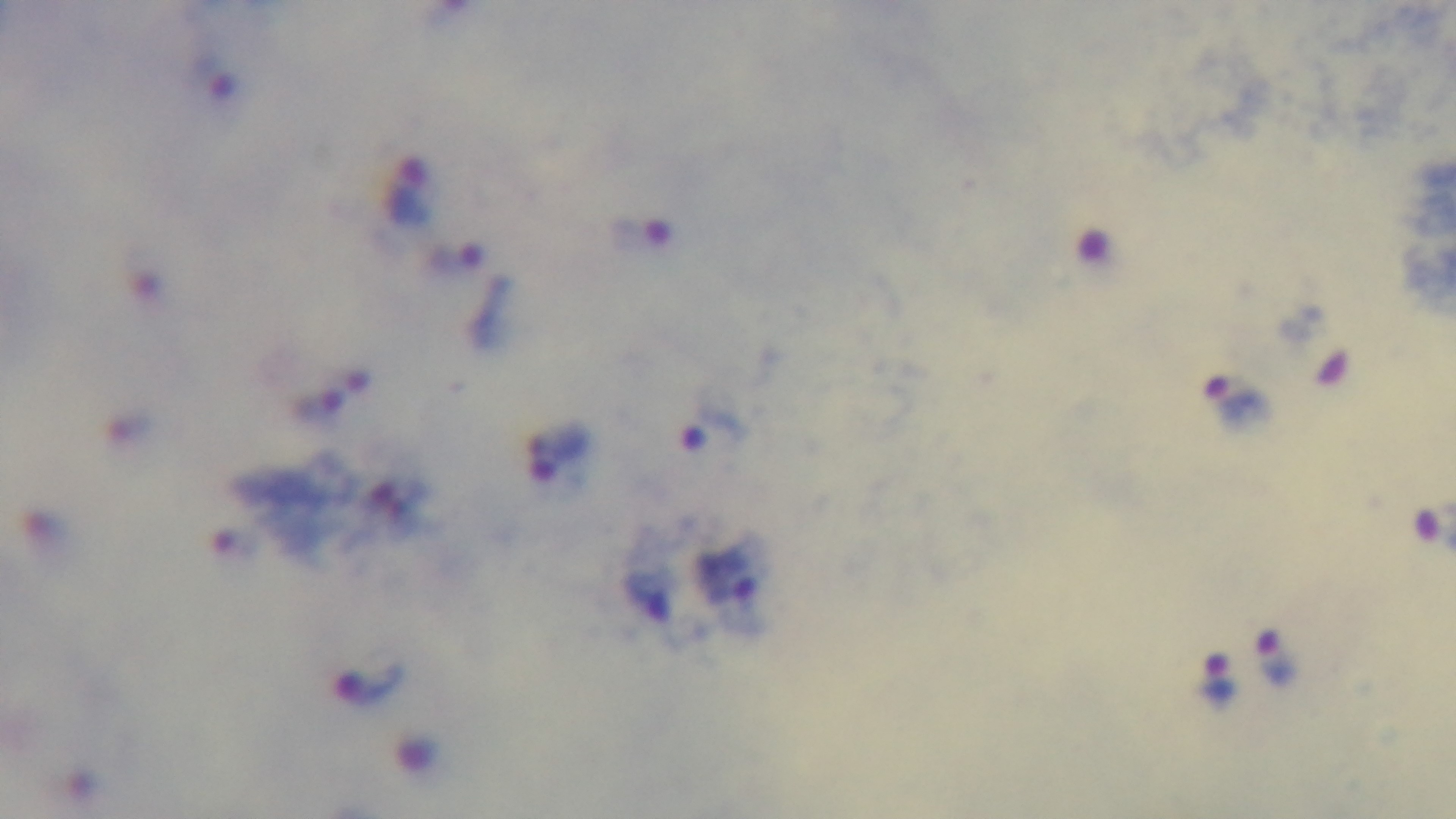
Summary:
  - Capture: mounted 4K digital camera
  - Stain: Giemsa
  - Objective: 100x oil immersion
  - Preparation: thick smear
  - Malaria status: infected
  - Field of view: one from the slide
  - Modality: light microscopy